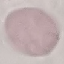
Malaria status: uninfected. Acquired by smartphone through the microscope eyepiece. Automatically extracted cell patch, resized to 64 × 64 pixels. Giemsa stain. Thin blood film.